Report the malaria status of this cell.
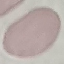

It is uninfected.

image type = automatically extracted cell patch, resized to 64 × 64 pixels
preparation = thin blood film
stain = Giemsa
capture = smartphone through the microscope eyepiece